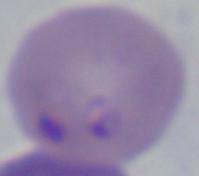
Summary:
  - Identification: Babesia
  - Magnification: 1000x
  - Modality: photomicrograph